Identify the blood parasite species.
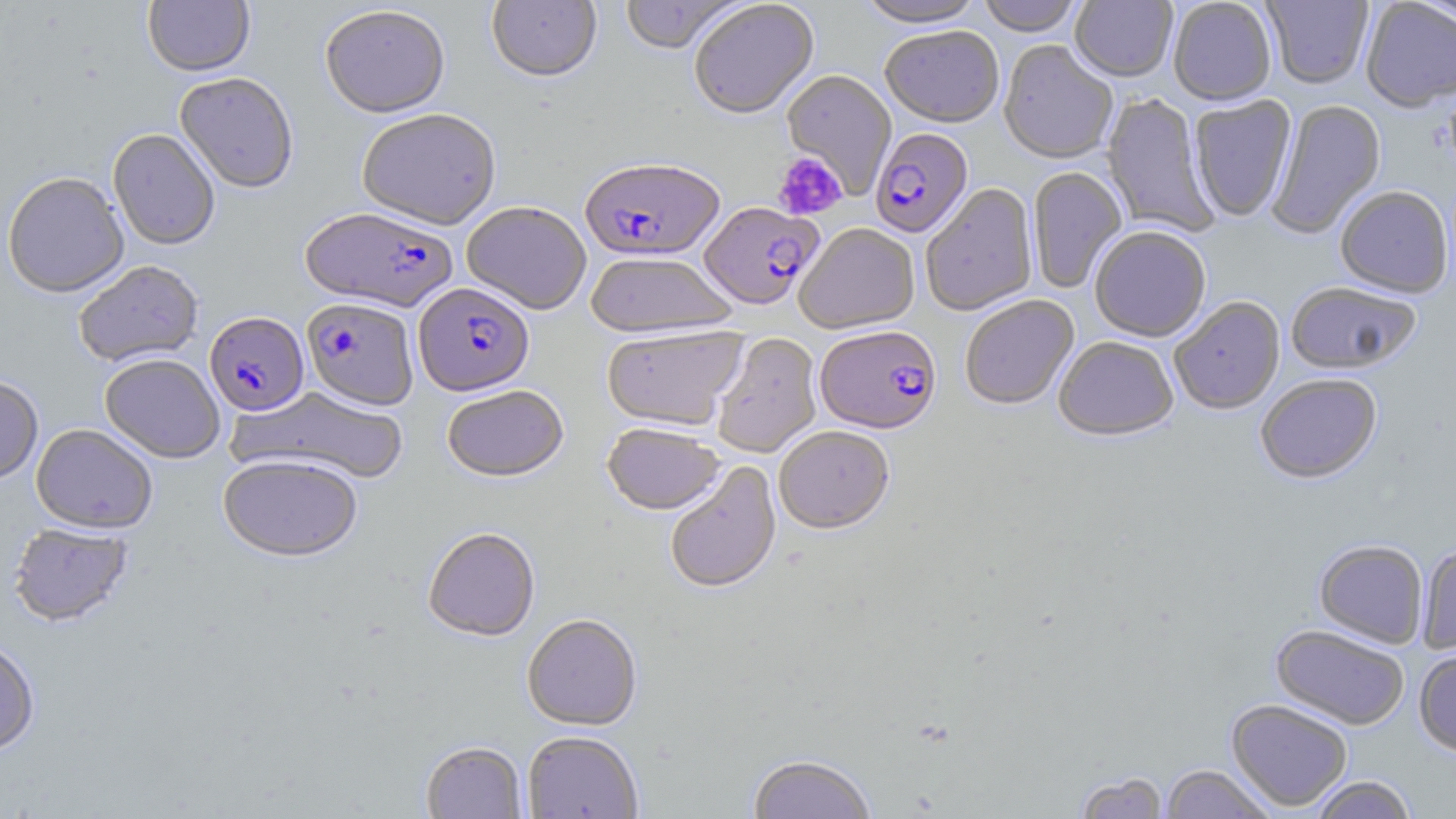
Plasmodium falciparum.

Summary:
  - Coordinate format: approximate bounding boxes as named x1/y1/x2/y2 corners in pixels
  - Plasmodium falciparum-infected red blood cell locations: (x1=869, y1=130, x2=973, y2=240), (x1=580, y1=159, x2=725, y2=264), (x1=699, y1=204, x2=824, y2=312), (x1=300, y1=210, x2=458, y2=314), (x1=413, y1=284, x2=535, y2=398), (x1=301, y1=300, x2=419, y2=414), (x1=205, y1=314, x2=309, y2=417), (x1=815, y1=327, x2=942, y2=436)
  - Platelet locations: (x1=773, y1=152, x2=847, y2=220)
  - Uninfected red blood cell locations: (x1=143, y1=0, x2=255, y2=79), (x1=619, y1=0, x2=748, y2=56), (x1=855, y1=0, x2=987, y2=31), (x1=977, y1=0, x2=1085, y2=38), (x1=1070, y1=0, x2=1177, y2=84), (x1=1168, y1=0, x2=1277, y2=107), (x1=1262, y1=0, x2=1373, y2=89), (x1=1415, y1=0, x2=1456, y2=30), (x1=486, y1=1, x2=602, y2=86), (x1=690, y1=1, x2=820, y2=122), (x1=1360, y1=1, x2=1456, y2=113), (x1=319, y1=7, x2=450, y2=121), (x1=880, y1=28, x2=1004, y2=130), (x1=999, y1=42, x2=1117, y2=166), (x1=781, y1=71, x2=897, y2=198), (x1=174, y1=75, x2=298, y2=195), (x1=1101, y1=93, x2=1218, y2=238), (x1=1189, y1=96, x2=1297, y2=223), (x1=1267, y1=99, x2=1386, y2=239), (x1=357, y1=111, x2=502, y2=232), (x1=108, y1=131, x2=220, y2=251), (x1=1027, y1=167, x2=1127, y2=292), (x1=1, y1=174, x2=129, y2=300), (x1=921, y1=185, x2=1039, y2=317), (x1=1335, y1=187, x2=1453, y2=300), (x1=461, y1=203, x2=591, y2=316), (x1=795, y1=225, x2=919, y2=336), (x1=1090, y1=228, x2=1211, y2=343), (x1=586, y1=253, x2=737, y2=341), (x1=73, y1=261, x2=205, y2=369), (x1=1285, y1=283, x2=1421, y2=376), (x1=960, y1=296, x2=1079, y2=411), (x1=1170, y1=297, x2=1286, y2=415), (x1=601, y1=326, x2=748, y2=433), (x1=713, y1=333, x2=822, y2=458), (x1=1054, y1=337, x2=1178, y2=443), (x1=100, y1=355, x2=225, y2=465), (x1=1256, y1=375, x2=1383, y2=486), (x1=0, y1=377, x2=43, y2=487), (x1=228, y1=386, x2=409, y2=484), (x1=442, y1=386, x2=569, y2=484), (x1=31, y1=424, x2=157, y2=536), (x1=602, y1=424, x2=725, y2=517), (x1=774, y1=427, x2=895, y2=537), (x1=218, y1=455, x2=361, y2=565), (x1=664, y1=462, x2=782, y2=596), (x1=8, y1=524, x2=134, y2=629), (x1=423, y1=529, x2=539, y2=644), (x1=1314, y1=540, x2=1428, y2=649), (x1=1417, y1=545, x2=1456, y2=654), (x1=521, y1=615, x2=642, y2=733), (x1=1271, y1=625, x2=1410, y2=730), (x1=0, y1=638, x2=39, y2=757), (x1=1414, y1=650, x2=1456, y2=757), (x1=1226, y1=700, x2=1353, y2=813), (x1=521, y1=732, x2=644, y2=818), (x1=421, y1=742, x2=527, y2=819), (x1=748, y1=756, x2=876, y2=819), (x1=1161, y1=765, x2=1276, y2=818), (x1=1073, y1=772, x2=1169, y2=819), (x1=1309, y1=776, x2=1417, y2=819)
  - Preparation: thin blood smear
  - Stain: May-Grünwald-Giemsa
  - Modality: light microscopy
  - Magnification: 1000x
  - Image size: 1456×819 pixels
  - Field of view: single